Report the malaria status of this cell.
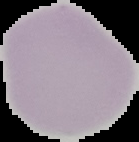
It is uninfected.

From a thin blood smear. The area outside the segmented cell region is set to black. Image is 139×142 pixels.